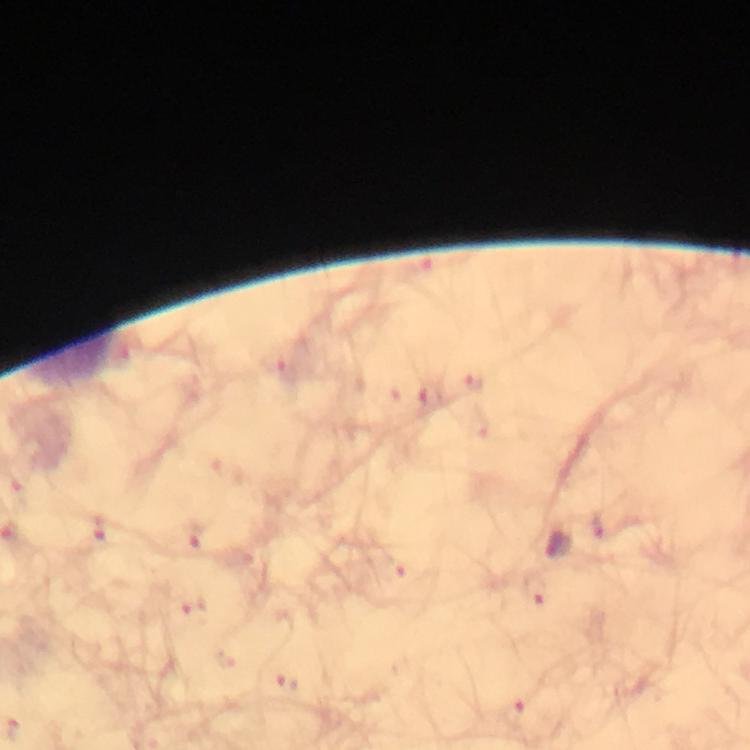

{
  "context": "from a diagnostic examination for malaria",
  "stain": "Giemsa",
  "malaria_parasite_locations": "approximate centers as (x, y) in pixels: (558, 545)",
  "magnification": "100x",
  "immersion_oil": "applied",
  "cropped_from": "one field of view",
  "preparation": "thick smear",
  "image_size": "750×750 pixels",
  "capture": "smartphone camera through the microscope"
}